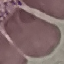
result = negative for malaria parasites
capture = smartphone camera at the microscope eyepiece
stain = Giemsa
preparation = thin blood smear
image type = automatically extracted cell patch, resized to 64 × 64 pixels